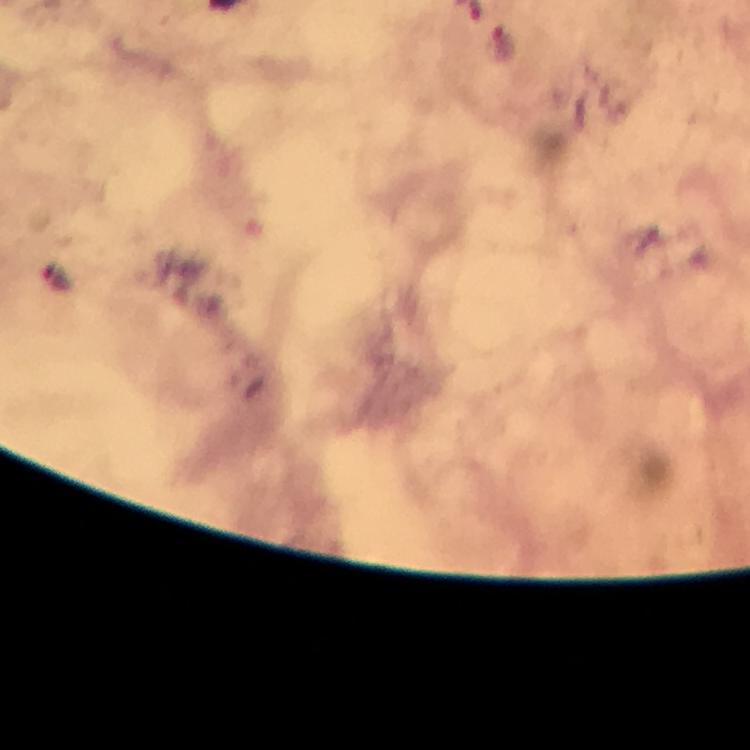

immersion oil = used
magnification = 100x
cropped from = a single field of view
Plasmodium parasite locations = approximate centers as [x, y] in pixels: [504, 46]
stain = Giemsa
context = from a malaria diagnostic workup
capture = smartphone photograph through a microscope
preparation = thick smear
image size = 750×750 pixels